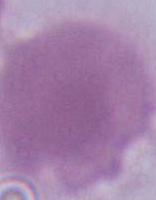
Photomicrograph. A red blood cell is seen. 1000x magnification.